State which cell type is depicted.
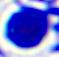
This is a leukocyte.

magnification = 400x
modality = photomicrograph